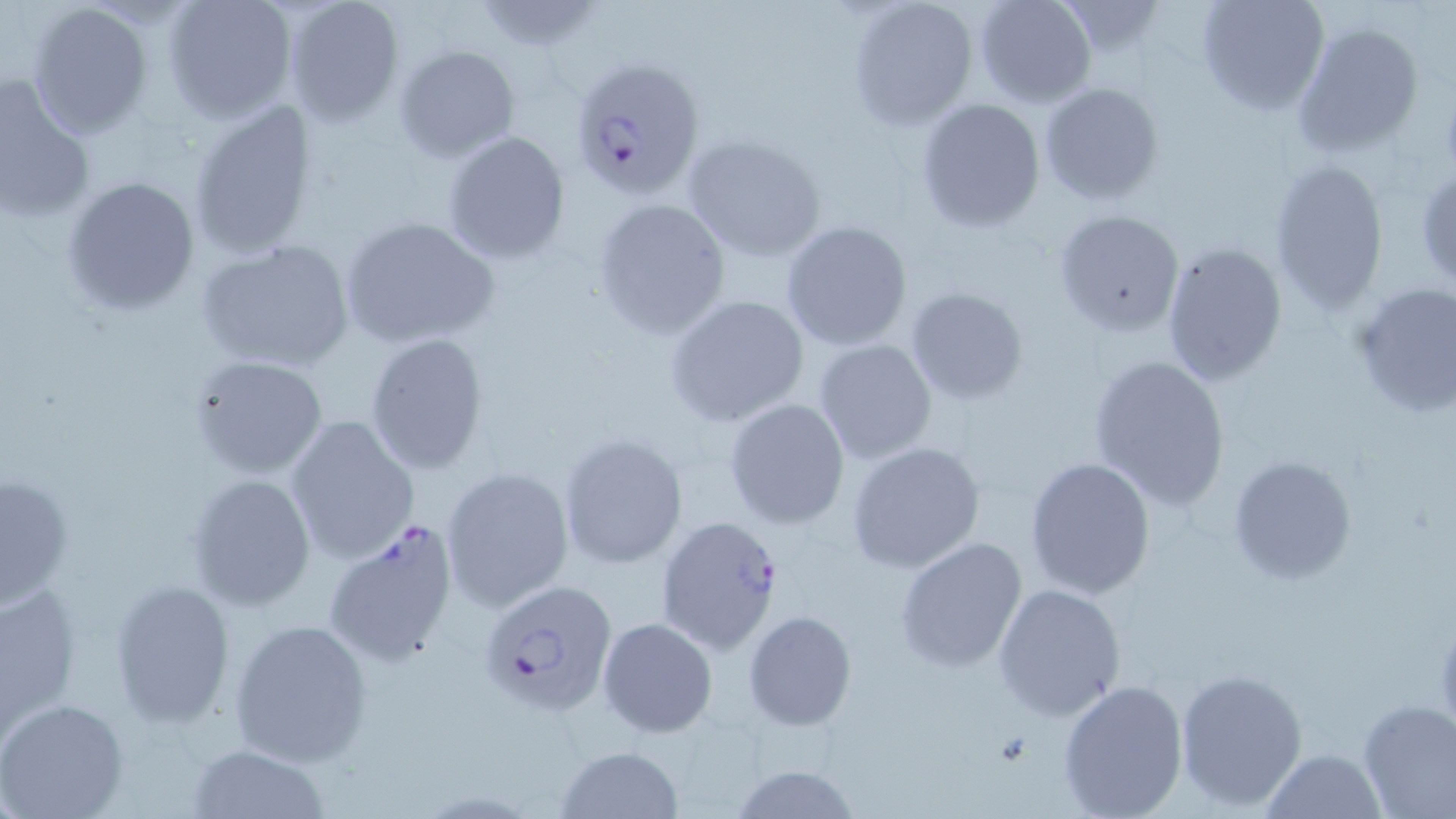
Approximate bounding boxes as (x1, y1, x2, y2) in pixels. Uninfected red blood cell locations: (161, 0, 297, 123), (283, 0, 406, 127), (848, 0, 979, 130), (974, 0, 1098, 108), (1195, 0, 1329, 116), (471, 1, 602, 51), (25, 2, 153, 140), (1290, 21, 1426, 158), (393, 45, 521, 162), (0, 78, 97, 225), (1039, 82, 1164, 204), (915, 97, 1045, 232), (186, 98, 322, 259), (441, 131, 570, 264), (683, 131, 825, 262), (1267, 159, 1390, 313), (1415, 164, 1456, 290), (63, 174, 200, 316), (592, 198, 731, 339), (1053, 208, 1186, 338), (340, 216, 499, 349), (779, 221, 915, 351), (195, 239, 356, 374), (1160, 241, 1289, 386), (1352, 281, 1455, 420), (904, 286, 1030, 407), (665, 293, 810, 427), (363, 330, 490, 475), (812, 338, 938, 465), (1087, 353, 1232, 512), (187, 355, 330, 479), (723, 398, 850, 530), (285, 415, 420, 564), (558, 432, 690, 570), (846, 441, 987, 573), (1227, 453, 1359, 585), (1022, 455, 1155, 600), (440, 465, 576, 612), (0, 468, 76, 612), (185, 473, 316, 610), (895, 536, 1028, 673), (0, 578, 82, 737), (108, 578, 235, 727), (993, 584, 1126, 722), (741, 611, 856, 730), (597, 617, 717, 739), (229, 618, 373, 765), (1174, 667, 1308, 811), (1056, 677, 1188, 819), (0, 698, 129, 819), (1356, 698, 1456, 818), (185, 743, 330, 819), (552, 745, 686, 819), (1263, 748, 1385, 819), (726, 764, 863, 819). Plasmodium falciparum-infected red blood cell locations: (569, 57, 705, 201), (655, 516, 784, 656), (320, 518, 461, 667), (471, 584, 619, 716). Slide-level diagnosis: Plasmodium falciparum. Image is 1456×819 pixels. May-Grünwald-Giemsa stain. Thin blood film. Single field of view. Optical microscopy. Captured at 1000x magnification.